Assess the morphology of the erythrocytes.
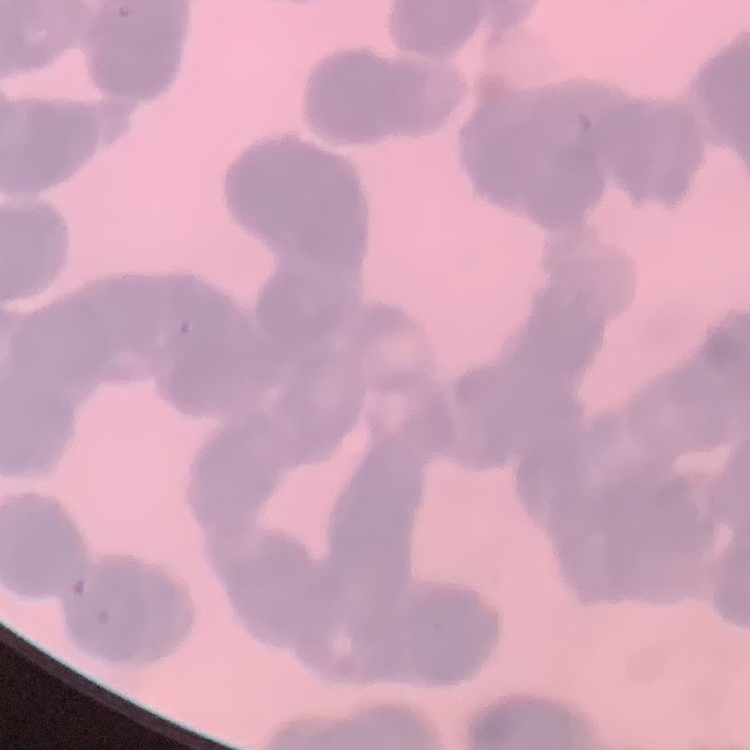
Rouleaux formation.

image_type: square crop of a larger photomicrograph
preparation: thin peripheral smear
stain: Field's or Giemsa